Assess this cell for malaria.
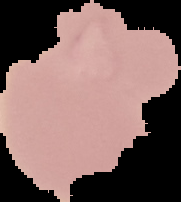
It is uninfected.

image size = 181×202 pixels
preparation = thin blood film
image type = segmented cell region on a black background